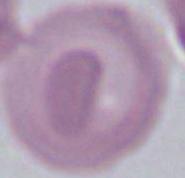
Summary:
  - Magnification: 1000x
  - Identification: erythrocyte
  - Modality: photomicrograph